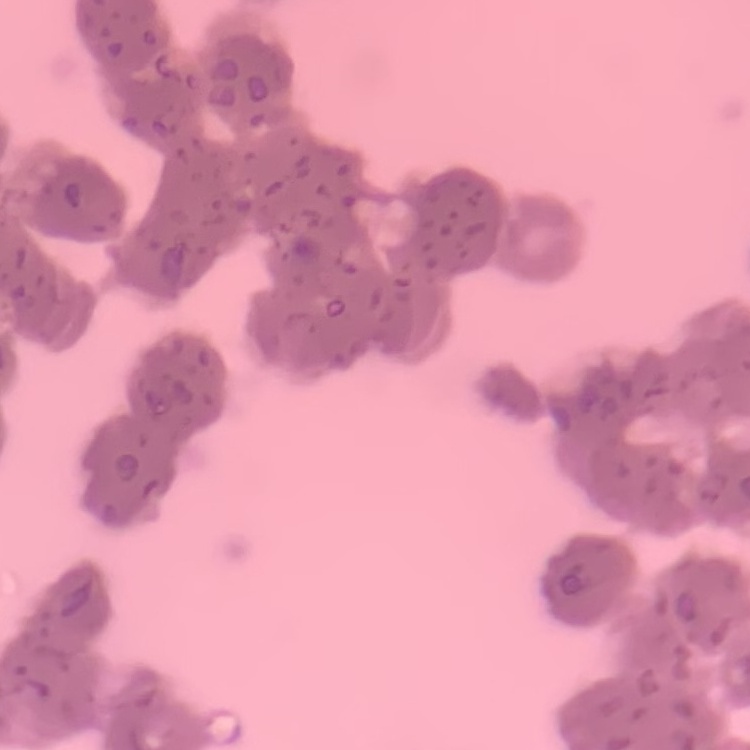
The erythrocytes show rouleaux formation. Square crop of a larger photomicrograph. Thin blood smear. Field's or Giemsa stain.